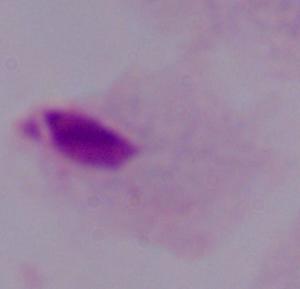
1000x magnification. A trichomonad is shown. Micrograph.